Comment on the morphology of the red blood cells.
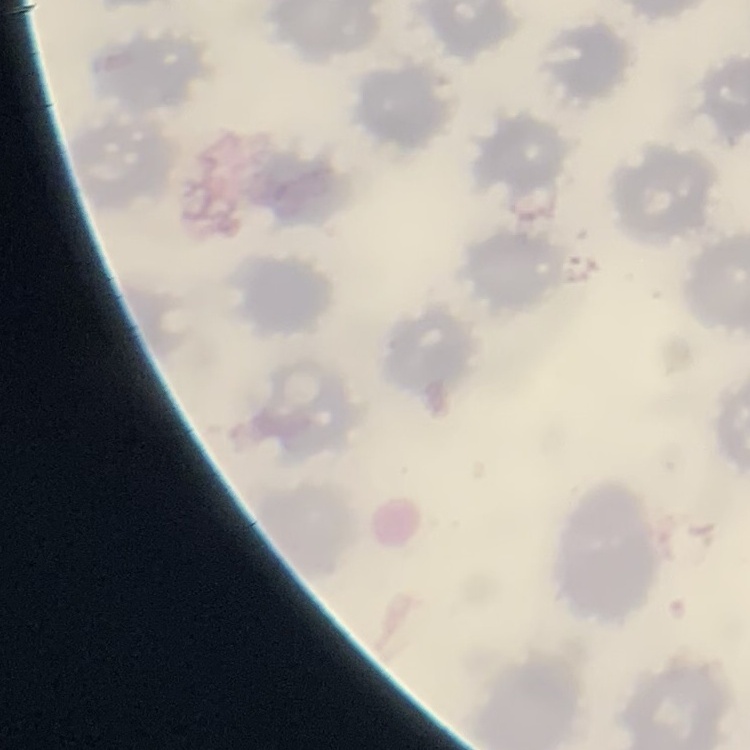
No rouleaux formation.

Summary:
  - Image type: square crop of a larger photomicrograph
  - Stain: Field's or Giemsa
  - Preparation: thin peripheral smear